Identify the cell.
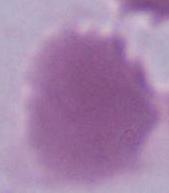
This is an erythrocyte.

Summary:
  - Magnification: 1000x
  - Modality: photomicrograph